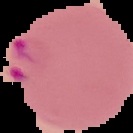
From a thin blood film. Malaria status: parasitized. Image is 133×133 pixels. Segmented cell region on a black background.